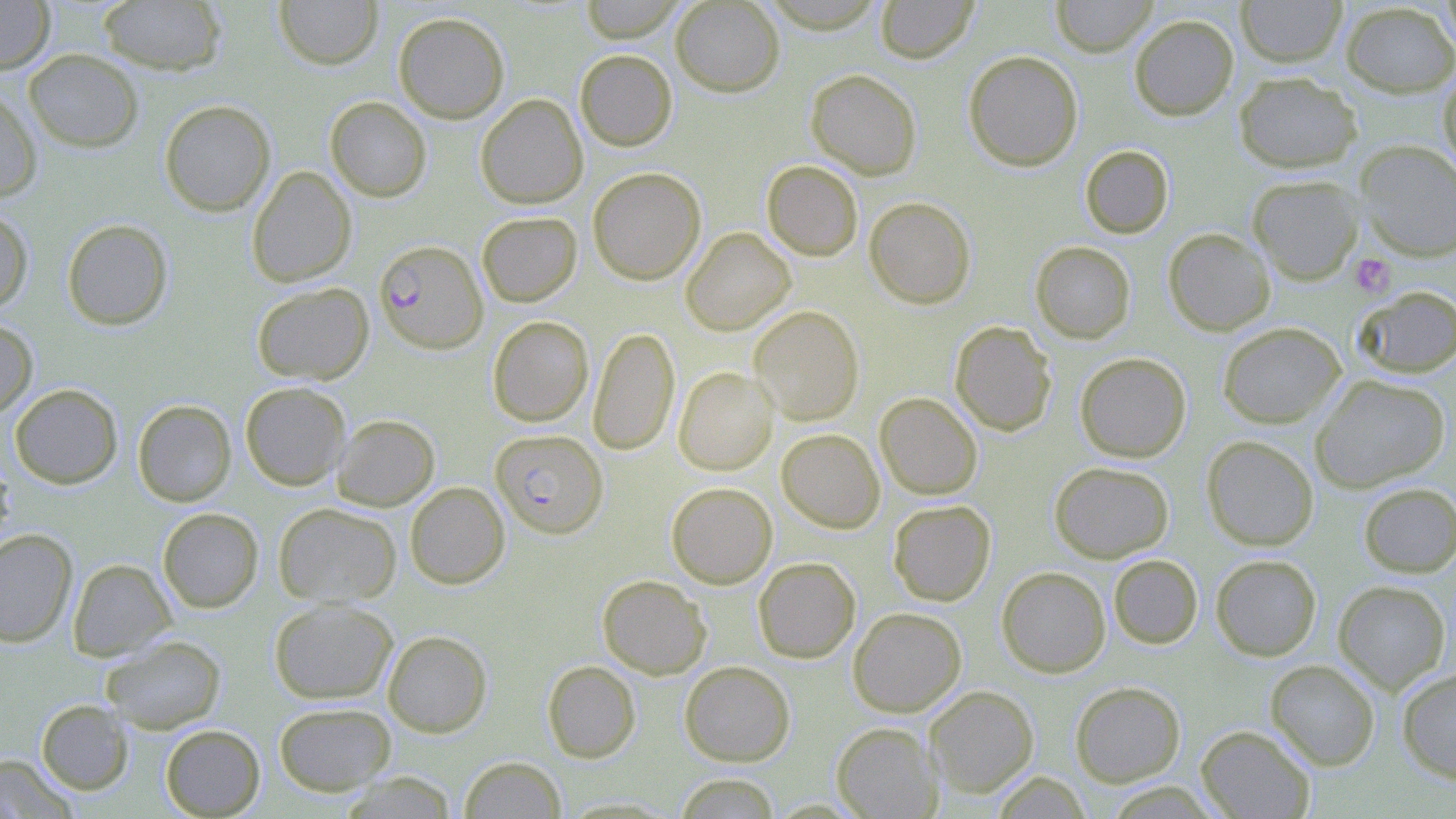

Summary:
  - Coordinate format: approximate bounding boxes as (x1,y1)-(x2,y2) corner pairs in pixels
  - Plasmodium falciparum-infected red blood cell locations: (374,239)-(488,353), (490,429)-(608,538)
  - Platelet locations: (1350,253)-(1397,298)
  - Uninfected red blood cell locations: (0,0)-(55,74), (273,0)-(383,69), (580,0)-(684,42), (670,0)-(784,96), (875,0)-(979,63), (1050,0)-(1158,56), (1235,0)-(1347,67), (1439,0)-(1456,54), (97,1)-(227,75), (1340,2)-(1456,97), (393,12)-(509,123), (1130,14)-(1239,120), (24,49)-(143,152), (575,49)-(677,151), (963,50)-(1083,171), (806,68)-(922,179), (1437,70)-(1456,178), (1233,71)-(1362,173), (0,84)-(42,203), (475,93)-(588,208), (325,96)-(432,201), (159,99)-(276,216), (1354,140)-(1456,261), (1079,145)-(1174,238), (762,160)-(863,261), (246,166)-(357,287), (588,167)-(706,285), (1247,176)-(1364,285), (864,196)-(976,308), (0,207)-(34,314), (477,211)-(582,306), (61,218)-(174,330), (681,227)-(795,335), (1162,228)-(1276,335), (1030,241)-(1135,343), (251,281)-(374,385), (1355,285)-(1456,378), (749,305)-(864,425), (487,315)-(594,426), (0,318)-(38,417), (949,320)-(1057,436), (1217,322)-(1346,428), (589,326)-(680,455), (1075,351)-(1191,462), (673,366)-(778,475), (1310,374)-(1450,492), (240,381)-(351,490), (10,383)-(123,489), (874,392)-(983,499), (133,399)-(236,506), (331,414)-(439,511), (776,428)-(885,533), (1202,435)-(1319,551), (0,450)-(15,549), (1049,461)-(1174,563), (405,482)-(509,588), (666,482)-(777,588), (1358,482)-(1456,577), (888,500)-(996,606), (273,502)-(402,608), (158,507)-(263,612), (0,528)-(77,647), (1210,553)-(1322,661), (1108,554)-(1203,649), (753,557)-(860,662), (68,558)-(175,661), (996,566)-(1110,677), (597,574)-(711,679), (1333,579)-(1451,694), (269,598)-(398,704), (848,606)-(966,716), (382,629)-(492,736), (101,635)-(226,733), (542,660)-(641,762), (1265,660)-(1381,770), (680,661)-(795,766), (1397,666)-(1456,783), (1070,681)-(1186,786), (924,686)-(1038,797), (36,699)-(133,794), (273,702)-(396,795), (831,721)-(943,818), (160,724)-(265,818), (1196,724)-(1316,819), (0,753)-(79,818), (459,756)-(566,818), (340,771)-(457,818), (992,772)-(1092,818), (674,773)-(782,818)
  - Slide-level diagnosis: Plasmodium falciparum
  - Field of view: single
  - Modality: light microscopy
  - Stain: May-Grünwald-Giemsa
  - Preparation: thin blood smear
  - Magnification: 1000x
  - Image size: 1456×819 pixels